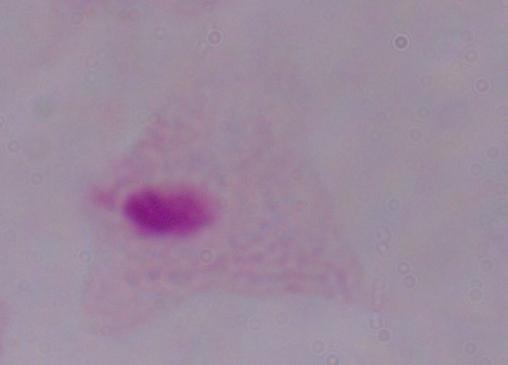 1000x magnification. Photomicrograph. A trichomonad is shown.